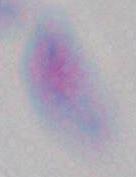

Captured at 1000x magnification. Photomicrograph. Toxoplasma gondii is shown.